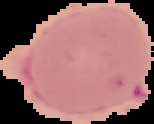 Malaria status: uninfected. From a thin blood smear. The area outside the segmented cell region is set to black. Image is 154×124 pixels.